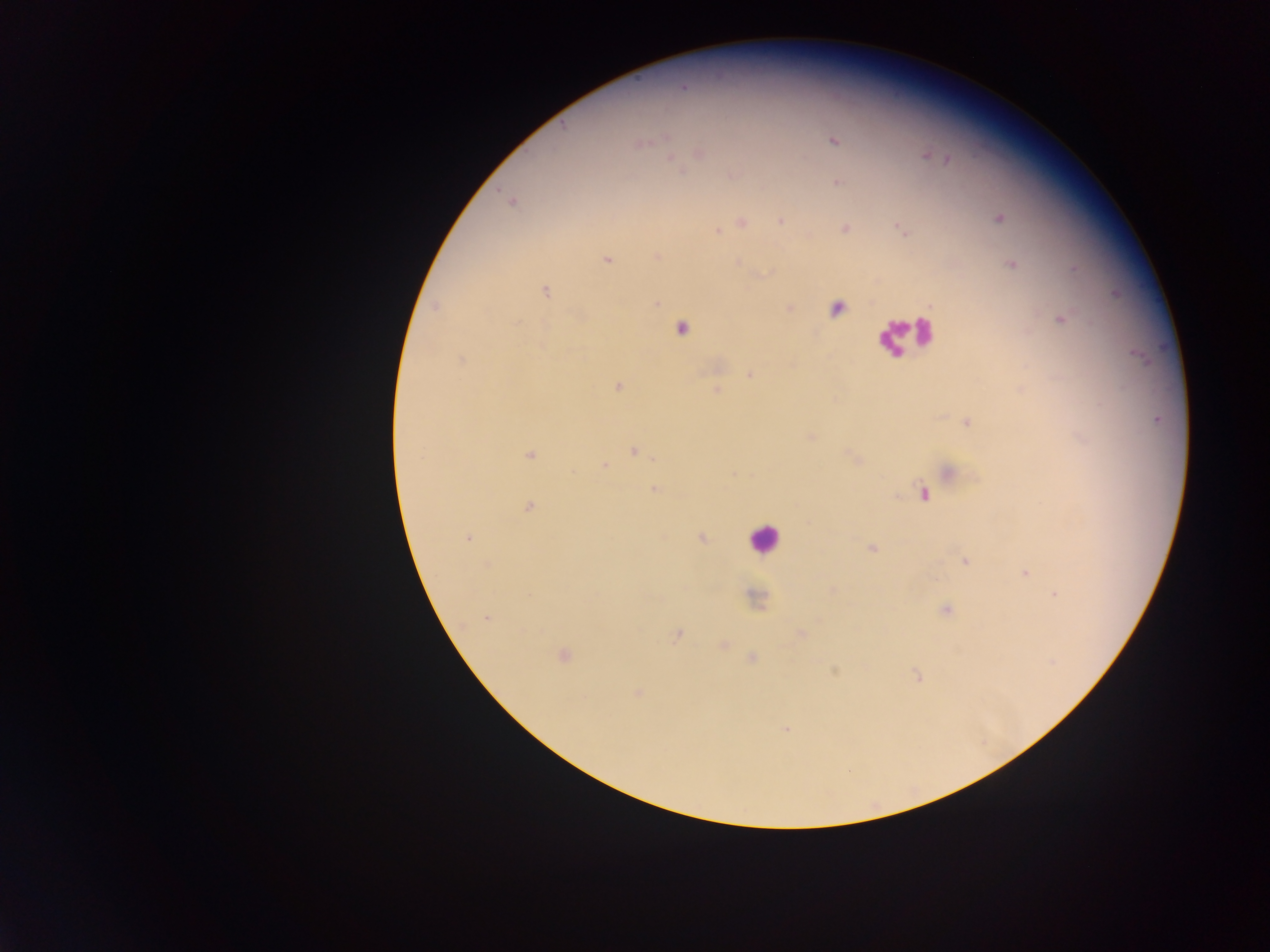

capture = mobile-phone photograph through a microscope
leukocyte locations = approximate centers as (x, y) in pixels: (907, 336), (764, 538)
field of view = single
Plasmodium parasite locations = approximate centers as (x, y) in pixels: (683, 86), (832, 140), (640, 143), (698, 153), (924, 154), (670, 157), (948, 159), (837, 183), (511, 201), (997, 217), (781, 221), (742, 222), (844, 228), (903, 230), (717, 231), (656, 257), (607, 259), (737, 262), (1011, 263), (545, 291), (654, 303), (436, 307), (836, 307), (789, 308), (1060, 319), (680, 328), (461, 360), (750, 375), (617, 386), (717, 390), (966, 422), (810, 437), (633, 450), (530, 454), (656, 456), (854, 458), (604, 466), (949, 470), (655, 489), (923, 494), (528, 507), (701, 537), (467, 538), (871, 548), (964, 560), (486, 565), (1025, 573), (830, 589), (1055, 594), (755, 598), (945, 609), (486, 616), (677, 634), (801, 634), (723, 645), (563, 655), (751, 658), (835, 671), (916, 676), (637, 693), (786, 729)
country = Ghana
image size = 1270×952 pixels
preparation = thick blood film